Comment on the morphology of the erythrocytes.
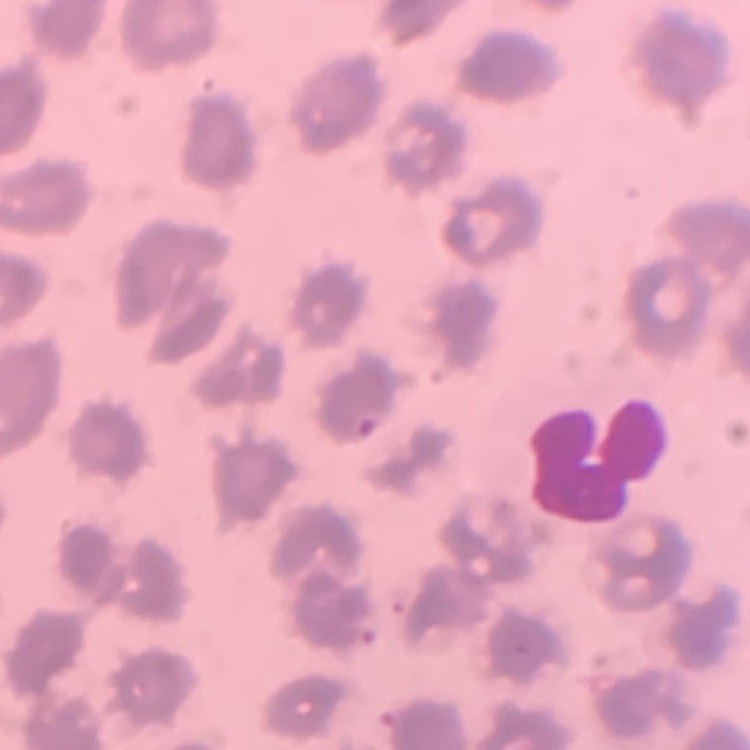
They show no rouleaux formation.

preparation: thin peripheral smear
image_type: square crop of a larger photomicrograph
stain: Field's or Giemsa